Name the parasite shown.
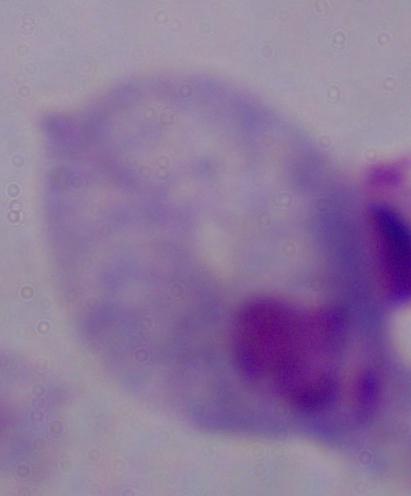
A trichomonad.

Summary:
  - Magnification: 1000x
  - Modality: micrograph